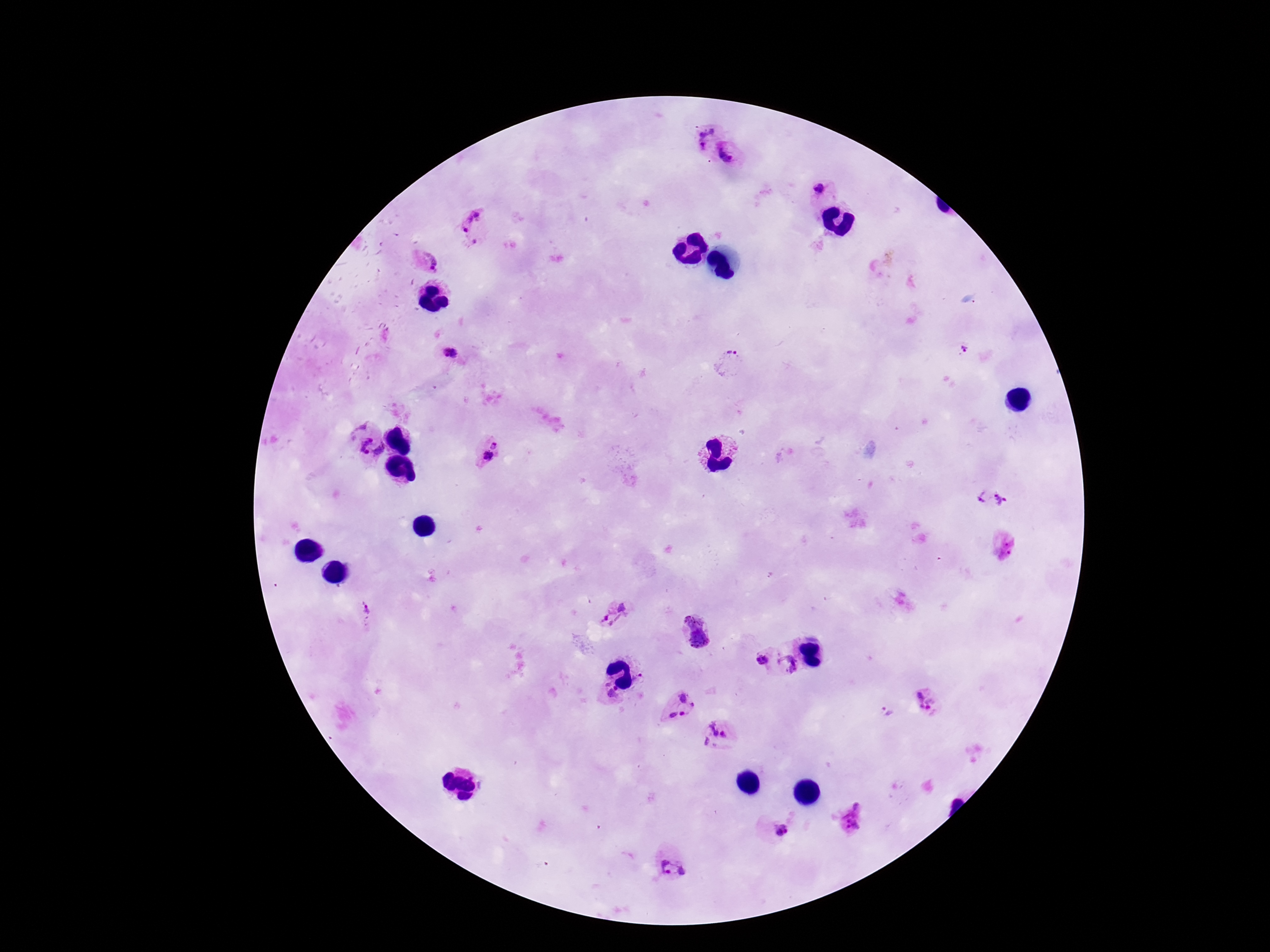

{
  "preparation": "thick blood film",
  "stain": "Giemsa",
  "patient_malaria_status": "positive",
  "capture": "smartphone camera through the microscope eyepiece",
  "magnification": "100x",
  "image_size": "1270×952 pixels",
  "plasmodium_parasite_locations": "approximate centers as (x, y) in pixels: (703, 136), (730, 153), (818, 190), (473, 226), (428, 263), (963, 352), (449, 354), (729, 361), (359, 439), (495, 444), (380, 450), (487, 456), (982, 496), (1002, 499), (1005, 546), (622, 607), (365, 609), (603, 616), (694, 619), (699, 639), (761, 659), (788, 664), (639, 678), (609, 693), (690, 697), (927, 699), (887, 712), (683, 714), (672, 715), (716, 735), (852, 817), (783, 831), (674, 870)",
  "field_of_view": "single"
}